Name the parasite shown.
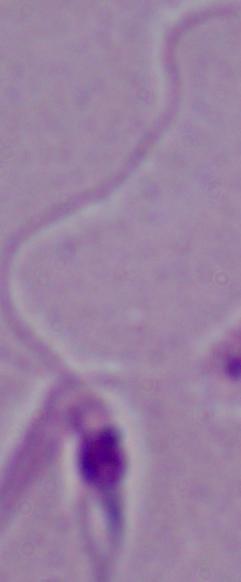
Leishmania.

Micrograph. 1000x magnification.